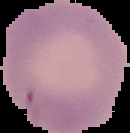
Image is 130×133 pixels. From a thin blood smear. Malaria status: uninfected. Cell region segmented out of the field of view; the surrounding area is masked to black.